Report the malaria status of this cell.
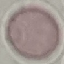

Uninfected.

Photographed with a smartphone camera at the microscope eyepiece. Cell patch, automatically extracted from a larger field of view and resized to 64 × 64 pixels. Thin blood smear. Giemsa-stained preparation.